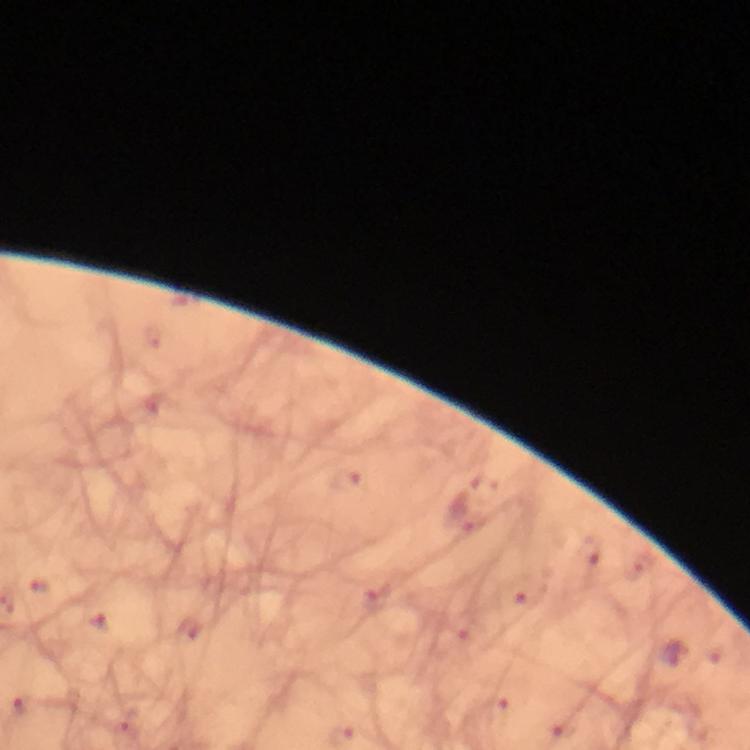

Approximate centers as (x, y) in pixels.
Summary:
  - Plasmodium parasite locations: (674, 653)
  - Immersion oil: applied
  - Image size: 750×750 pixels
  - Cropped from: a single field of view
  - Stain: Giemsa
  - Magnification: 100x
  - Context: from a diagnostic examination for malaria
  - Capture: smartphone camera through the microscope
  - Preparation: thick blood smear